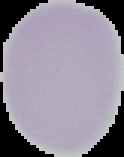

Result: no malaria parasites detected. From a thin blood film. Image is 124×157 pixels. Cell region segmented out of the field of view; the surrounding area is masked to black.